Report the malaria status of this cell.
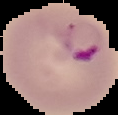

Parasitized.

Summary:
  - Image size: 118×115 pixels
  - Preparation: thin blood film
  - Image type: cell region segmented out of the field of view; surrounding area masked to black